Assess this cell for malaria.
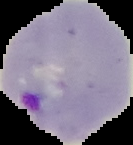
It is parasitized.

Cell region segmented out of the field of view; the surrounding area is masked to black. From a thin blood smear. Image is 133×145 pixels.